Locate every blood parasite and identify its species.
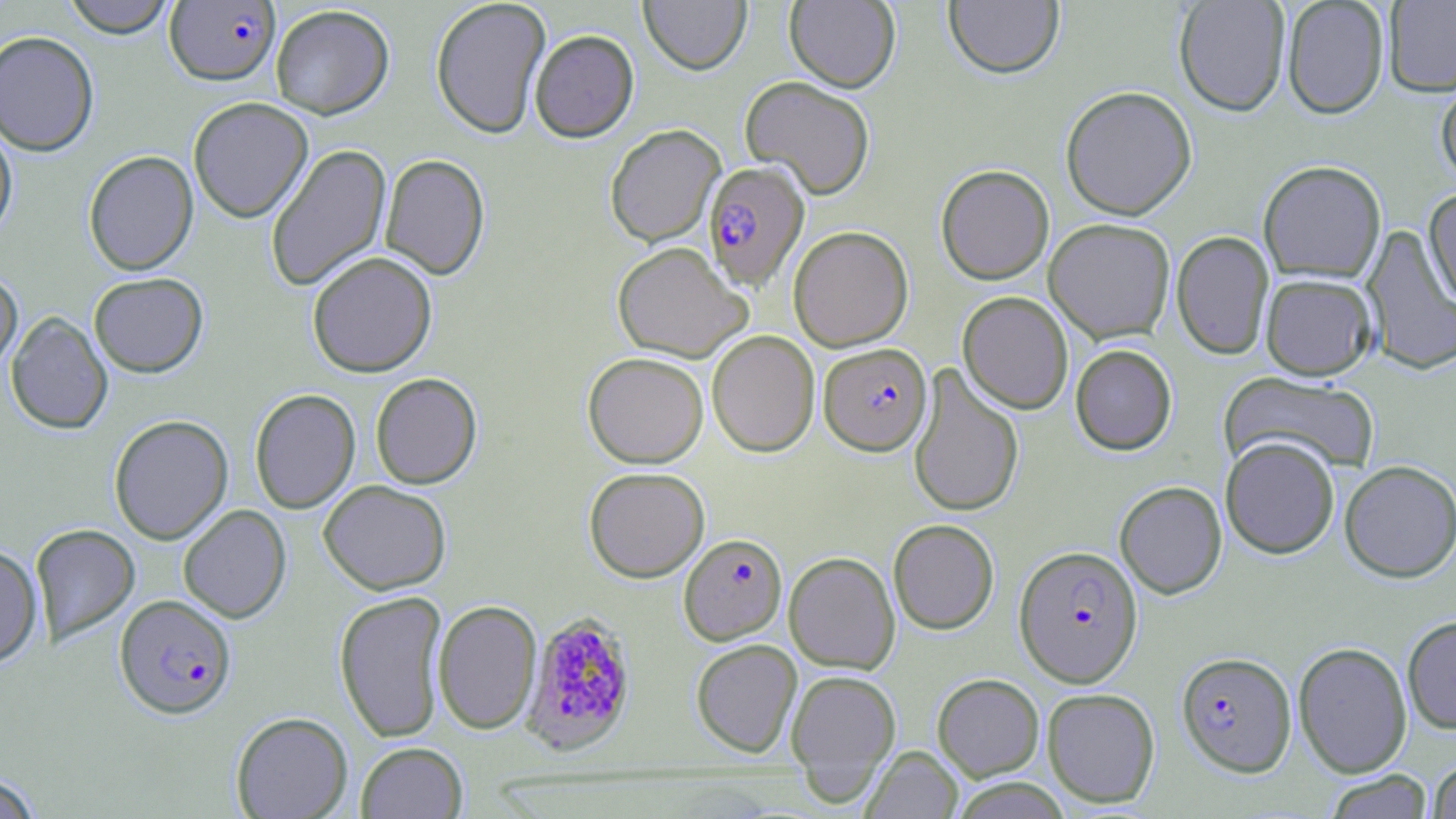

Approximate bounding boxes as [x1, y1, x2, y2] in pixels.
Plasmodium falciparum-infected red blood cells: [164, 1, 280, 86], [703, 161, 809, 291], [819, 343, 932, 456], [679, 533, 787, 645], [1014, 545, 1143, 686], [115, 594, 236, 718], [519, 610, 638, 754], [1176, 651, 1297, 777].
No Plasmodium ovale, Plasmodium malariae, Plasmodium vivax, Babesia divergens, or Trypanosoma brucei observed.

Summary:
  - Uninfected red blood cell locations: [61, 0, 179, 38], [430, 0, 551, 139], [639, 0, 751, 75], [944, 0, 1064, 79], [1383, 0, 1456, 97], [784, 1, 900, 92], [1173, 1, 1290, 116], [1281, 1, 1389, 119], [270, 5, 394, 119], [529, 29, 639, 142], [0, 30, 99, 155], [1435, 74, 1456, 188], [740, 76, 876, 200], [1060, 85, 1197, 220], [188, 96, 313, 223], [0, 117, 18, 243], [605, 124, 725, 247], [265, 143, 392, 292], [83, 150, 199, 275], [380, 153, 490, 280], [1258, 160, 1387, 284], [936, 165, 1054, 284], [1423, 187, 1456, 312], [1044, 218, 1175, 343], [788, 225, 913, 351], [1361, 225, 1456, 375], [1171, 231, 1274, 360], [612, 241, 752, 363], [307, 251, 437, 377], [0, 269, 23, 374], [89, 272, 208, 377], [1261, 273, 1377, 380], [957, 291, 1073, 414], [6, 311, 113, 434], [707, 329, 820, 457], [1070, 344, 1177, 455], [583, 351, 708, 468], [908, 363, 1024, 518], [1220, 371, 1381, 477], [370, 372, 483, 489], [249, 388, 361, 514], [109, 414, 233, 545], [1220, 436, 1340, 559], [1339, 460, 1456, 582], [584, 466, 710, 582], [318, 480, 451, 595], [1115, 480, 1227, 598], [178, 504, 291, 623], [888, 519, 999, 634], [30, 523, 140, 646], [0, 544, 43, 667], [784, 551, 900, 674], [334, 590, 449, 743], [433, 600, 542, 735], [1402, 614, 1456, 734], [691, 639, 802, 758], [1293, 641, 1412, 778], [785, 669, 901, 789], [932, 673, 1044, 781], [1042, 687, 1160, 808], [231, 711, 353, 818], [356, 742, 468, 818], [862, 745, 963, 818], [1427, 759, 1456, 818], [1323, 770, 1433, 818], [0, 773, 43, 818], [949, 778, 1073, 818]
  - Slide-level diagnosis: Plasmodium falciparum
  - Field of view: one of a larger specimen
  - Stain: May-Grünwald-Giemsa
  - Image size: 1456×819 pixels
  - Magnification: 1000x
  - Preparation: thin blood smear
  - Modality: optical microscopy